Assess this cell for malaria.
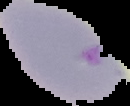

Parasitized.

preparation = thin blood smear
image type = segmented cell region on a black background
image size = 130×106 pixels